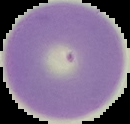

Summary:
  - Preparation: thin blood smear
  - Image type: cell region segmented out of the field of view; surrounding area masked to black
  - Image size: 130×124 pixels
  - Result: negative for malaria parasites